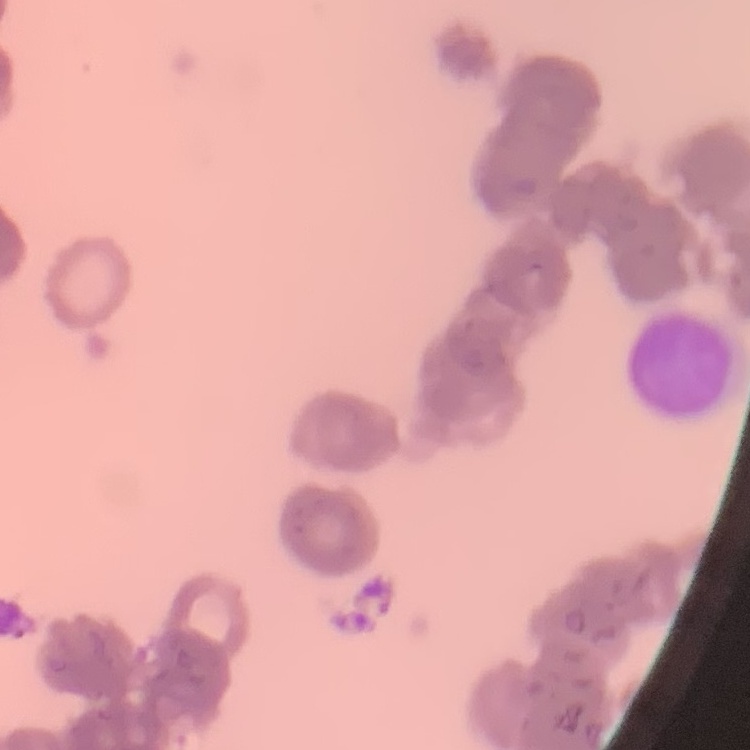
erythrocyte morphology = rouleaux formation
image type = square crop of a larger photomicrograph
stain = Field's or Giemsa
preparation = thin blood smear